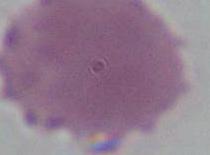

Summary:
  - Modality: micrograph
  - Identification: red blood cell
  - Magnification: 1000x